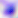

Summary:
  - Modality: micrograph
  - Identification: Toxoplasma gondii
  - Magnification: 400x